Describe the morphology of the erythrocytes.
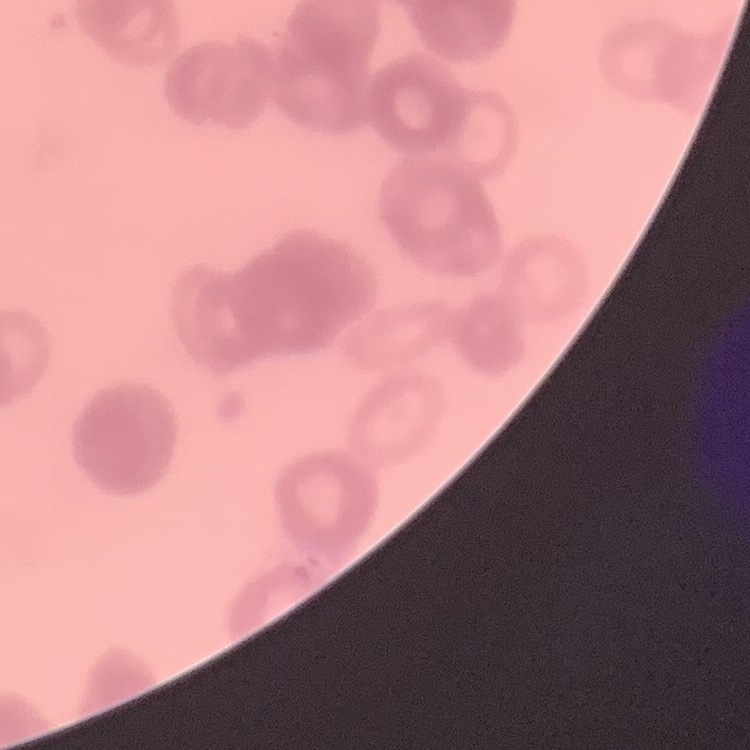
They show rouleaux formation.

Summary:
  - Image type: square crop of a larger photomicrograph
  - Stain: Field's or Giemsa
  - Preparation: thin blood smear